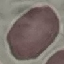

{
  "malaria_status": "uninfected",
  "capture": "smartphone camera at the microscope eyepiece",
  "preparation": "thin blood film",
  "stain": "Giemsa",
  "image_type": "cell patch, automatically extracted from a larger field of view and resized to 64 × 64 pixels"
}